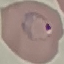 Malaria status: parasitized. Giemsa-stained preparation. Cell patch, automatically extracted from a larger field of view and resized to 64 × 64 pixels. Thin blood film. Photographed with a smartphone camera at the microscope eyepiece.